Locate every blood parasite and identify its species.
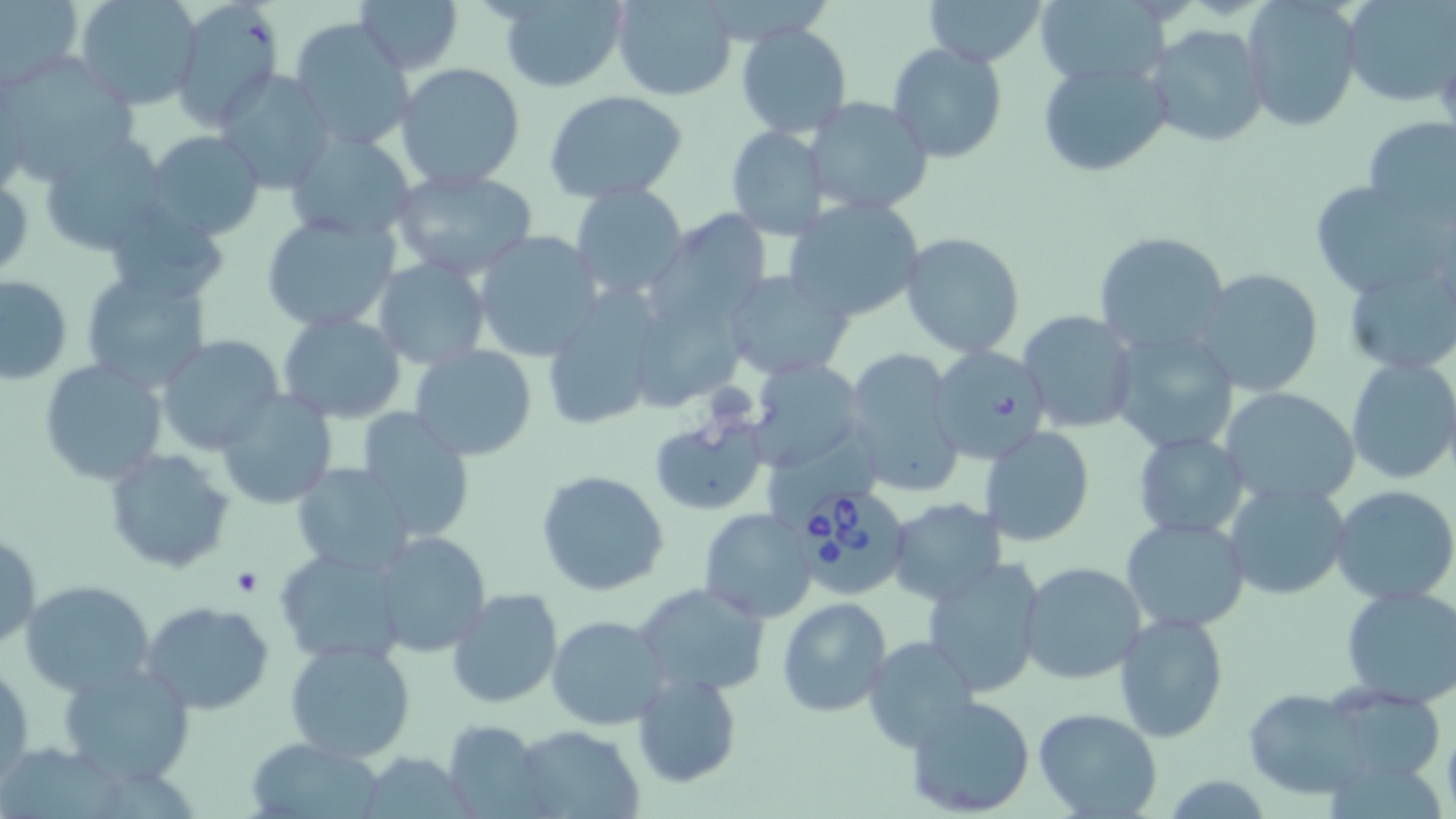
Approximate bounding boxes as (x1, y1, x2, y2) in pixels.
Babesia divergens-infected red blood cells: (786, 485, 913, 603).
No Plasmodium falciparum, Plasmodium ovale, Plasmodium malariae, Plasmodium vivax, or Trypanosoma brucei observed.

slide-level diagnosis = Babesia divergens
stain = May-Grünwald-Giemsa
image size = 1456×819 pixels
modality = light microscopy
magnification = 1000x
preparation = thin blood film
field of view = single
platelet locations = approximate bounding boxes as (x1, y1, x2, y2) in pixels: (233, 569, 264, 596)
uninfected red blood cell locations = approximate bounding boxes as (x1, y1, x2, y2) in pixels: (74, 0, 202, 111), (168, 0, 284, 127), (356, 0, 462, 76), (499, 0, 627, 91), (612, 0, 737, 100), (923, 0, 1047, 66), (1033, 0, 1171, 86), (1344, 0, 1456, 106), (1, 1, 82, 85), (1242, 1, 1363, 132), (289, 18, 415, 155), (735, 23, 853, 138), (1145, 24, 1271, 149), (886, 41, 1008, 164), (3, 54, 139, 183), (1036, 56, 1174, 177), (397, 62, 525, 191), (217, 71, 336, 194), (544, 91, 688, 205), (804, 95, 933, 220), (1360, 115, 1456, 230), (725, 124, 831, 238), (284, 128, 418, 241), (144, 130, 266, 241), (39, 136, 171, 258), (388, 166, 540, 281), (1310, 181, 1448, 299), (570, 182, 688, 300), (783, 198, 925, 323), (101, 203, 229, 305), (650, 210, 775, 333), (259, 212, 404, 333), (899, 231, 1027, 358), (472, 232, 602, 361), (1093, 232, 1231, 357), (373, 258, 489, 370), (1342, 258, 1456, 378), (81, 268, 212, 392), (1192, 269, 1324, 397), (724, 270, 853, 379), (0, 274, 72, 383), (629, 293, 741, 409), (540, 296, 661, 431), (1018, 310, 1138, 433), (277, 312, 406, 423), (1109, 327, 1240, 455), (154, 334, 284, 454), (409, 345, 538, 462), (926, 345, 1051, 465), (842, 348, 964, 497), (1345, 356, 1456, 486), (747, 358, 866, 471), (39, 359, 167, 485), (1220, 385, 1360, 509), (215, 390, 337, 510), (357, 407, 476, 539), (649, 414, 768, 516), (978, 425, 1096, 548), (1132, 432, 1250, 539), (104, 448, 237, 572), (293, 463, 415, 576), (538, 470, 669, 597), (1224, 481, 1351, 601), (1330, 486, 1455, 604), (886, 498, 1006, 606), (698, 509, 817, 623), (1121, 515, 1248, 633), (370, 531, 491, 658), (2, 532, 41, 648), (276, 545, 410, 667), (920, 560, 1047, 697), (1018, 561, 1146, 684), (21, 580, 155, 699), (634, 582, 771, 700), (1339, 584, 1456, 707), (446, 588, 563, 710), (775, 598, 891, 719), (142, 600, 272, 715), (1114, 611, 1229, 743), (547, 615, 670, 731), (863, 636, 980, 752), (285, 639, 416, 763), (56, 660, 194, 785), (1, 663, 33, 784), (630, 670, 742, 789), (1243, 690, 1376, 800), (903, 695, 1037, 818), (1035, 708, 1163, 818), (439, 721, 547, 814), (510, 725, 644, 819), (248, 735, 386, 818), (1156, 775, 1280, 816)